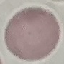

Malaria status: uninfected. Giemsa stain. Acquired by smartphone through the microscope eyepiece. Automatically extracted cell patch, resized to 64 × 64 pixels. Thin blood film.